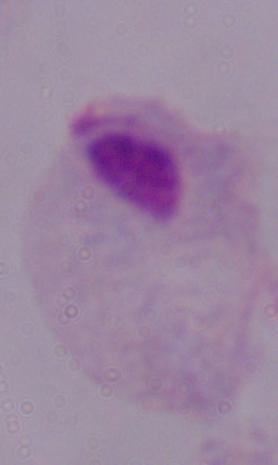
1000x magnification. A trichomonad is seen. Micrograph.